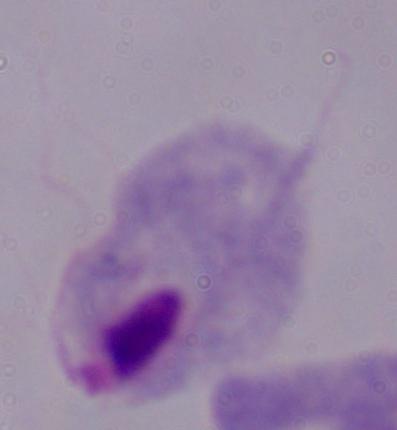

A trichomonad is shown. Captured at 1000x magnification. Photomicrograph.